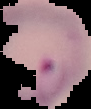
image type = segmented cell region with the area outside set to black
image size = 91×109 pixels
preparation = thin blood smear
result = Plasmodium parasites detected